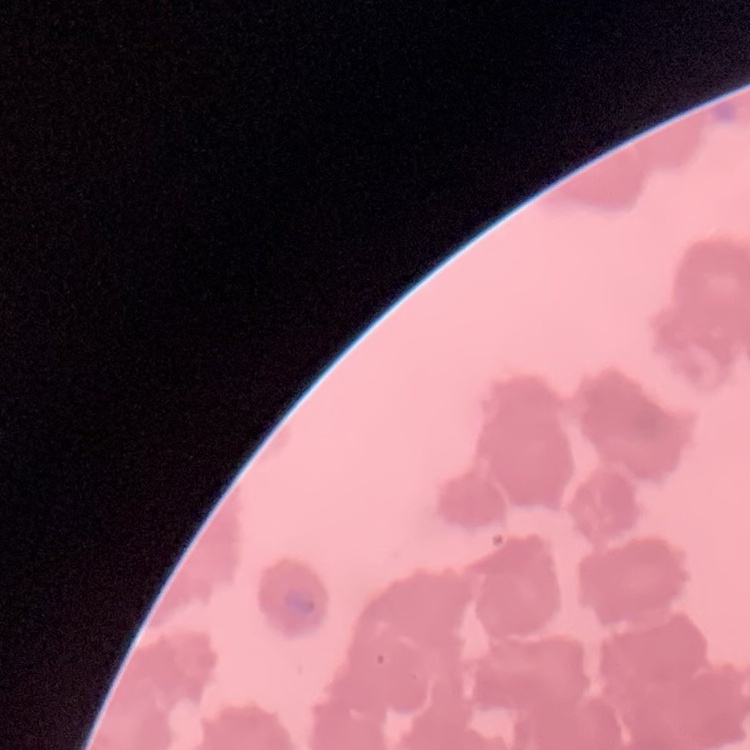

erythrocyte_morphology: rouleaux formation
preparation: thin blood smear
image_type: square crop of a larger photomicrograph
stain: Field's or Giemsa